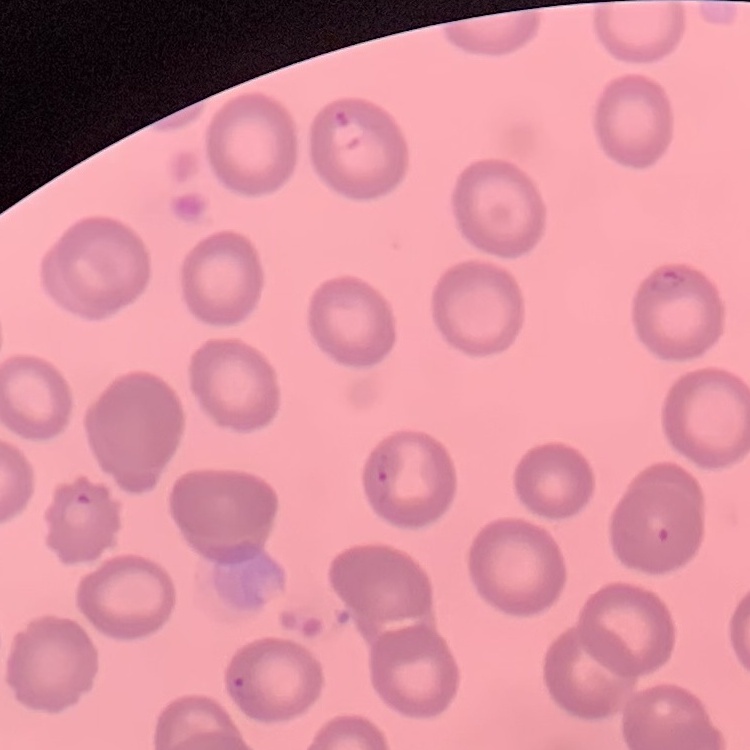
erythrocyte morphology = no rouleaux formation
image type = one tile cut from a larger photomicrograph
stain = Field's or Giemsa
preparation = thin blood film